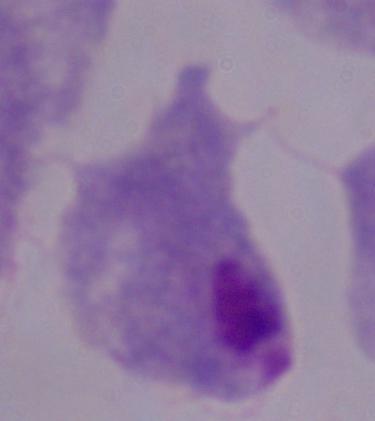
magnification = 1000x
identification = trichomonad
modality = micrograph